Identify the blood parasite species.
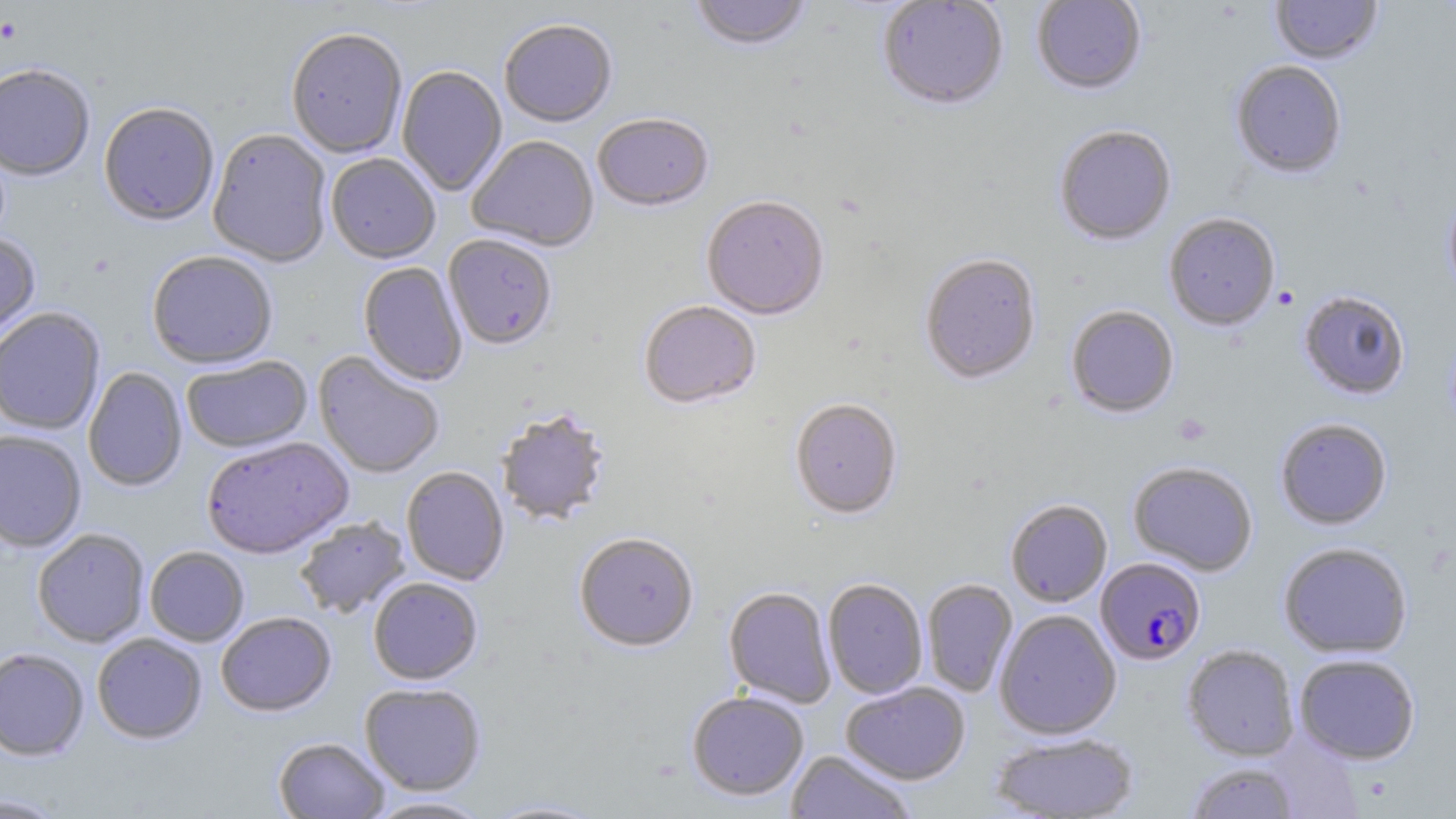

Plasmodium falciparum.

Approximate bounding boxes as (x1, y1, x2, y2) in pixels. Uninfected red blood cell locations: (689, 0, 814, 54), (1031, 0, 1146, 97), (1270, 0, 1383, 66), (877, 1, 1009, 112), (500, 21, 617, 128), (286, 30, 407, 160), (1230, 62, 1347, 180), (397, 66, 507, 197), (0, 67, 95, 183), (99, 104, 219, 228), (592, 115, 714, 214), (1054, 127, 1176, 246), (207, 130, 332, 268), (467, 137, 598, 253), (326, 155, 441, 265), (1442, 188, 1456, 301), (701, 198, 829, 322), (1164, 213, 1280, 331), (0, 234, 41, 345), (443, 236, 557, 351), (146, 253, 278, 370), (919, 255, 1041, 386), (358, 263, 467, 387), (1298, 290, 1411, 400), (639, 302, 761, 411), (1066, 306, 1179, 418), (0, 308, 107, 436), (313, 351, 444, 479), (181, 356, 313, 454), (83, 367, 188, 492), (790, 399, 903, 521), (496, 410, 611, 527), (1275, 418, 1393, 530), (0, 431, 86, 552), (201, 438, 354, 560), (1128, 461, 1258, 576), (401, 467, 509, 586), (1006, 499, 1112, 608), (295, 517, 411, 619), (32, 530, 149, 648), (574, 534, 699, 653), (1277, 541, 1413, 659), (145, 547, 249, 647), (368, 578, 483, 686), (823, 579, 928, 699), (922, 579, 1017, 697), (723, 588, 836, 708), (994, 609, 1121, 740), (216, 613, 336, 717), (92, 634, 207, 744), (1182, 644, 1299, 761), (0, 649, 89, 761), (1293, 653, 1421, 764), (841, 681, 970, 785), (360, 684, 486, 796), (687, 692, 808, 801), (991, 732, 1139, 818), (274, 738, 390, 818), (786, 751, 917, 818), (1184, 762, 1301, 818), (0, 793, 68, 818), (363, 796, 494, 818), (481, 798, 609, 818). Plasmodium falciparum-infected red blood cell locations: (1095, 557, 1207, 666). Platelet locations: (0, 18, 22, 46), (1172, 413, 1212, 446). Single field of view. Captured at 1000x magnification. May-Grünwald-Giemsa-stained preparation. Thin blood film. Optical microscopy. Image is 1456×819 pixels.